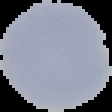
image_type: segmented cell region on a black background
preparation: thin blood film
result: no Plasmodium parasites seen
image_size: 112×112 pixels